Assess the morphology of the erythrocytes.
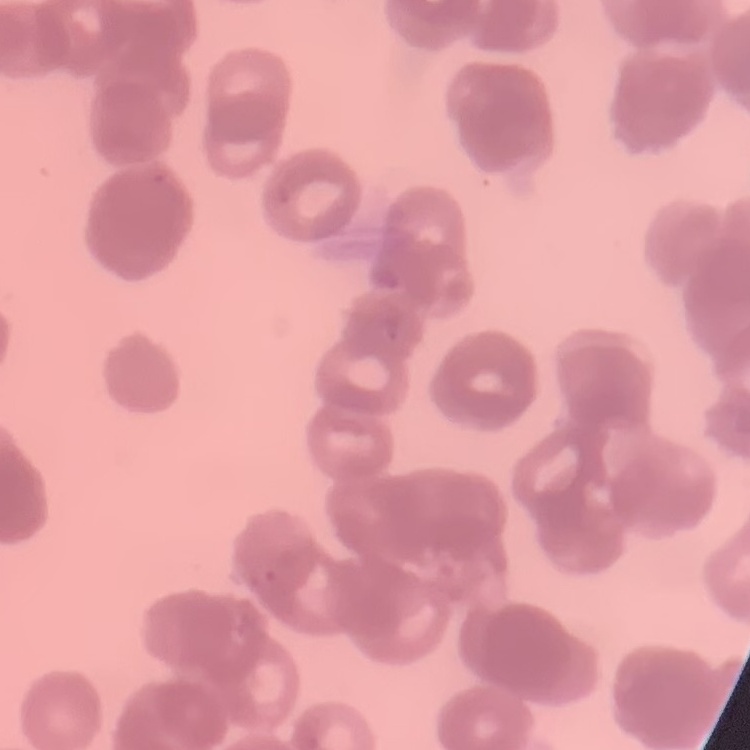
Rouleaux formation.

stain = Field's or Giemsa
image type = square crop of a larger photomicrograph
preparation = thin blood smear